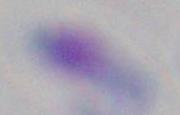
Photomicrograph. 1000x magnification. Toxoplasma gondii is seen.